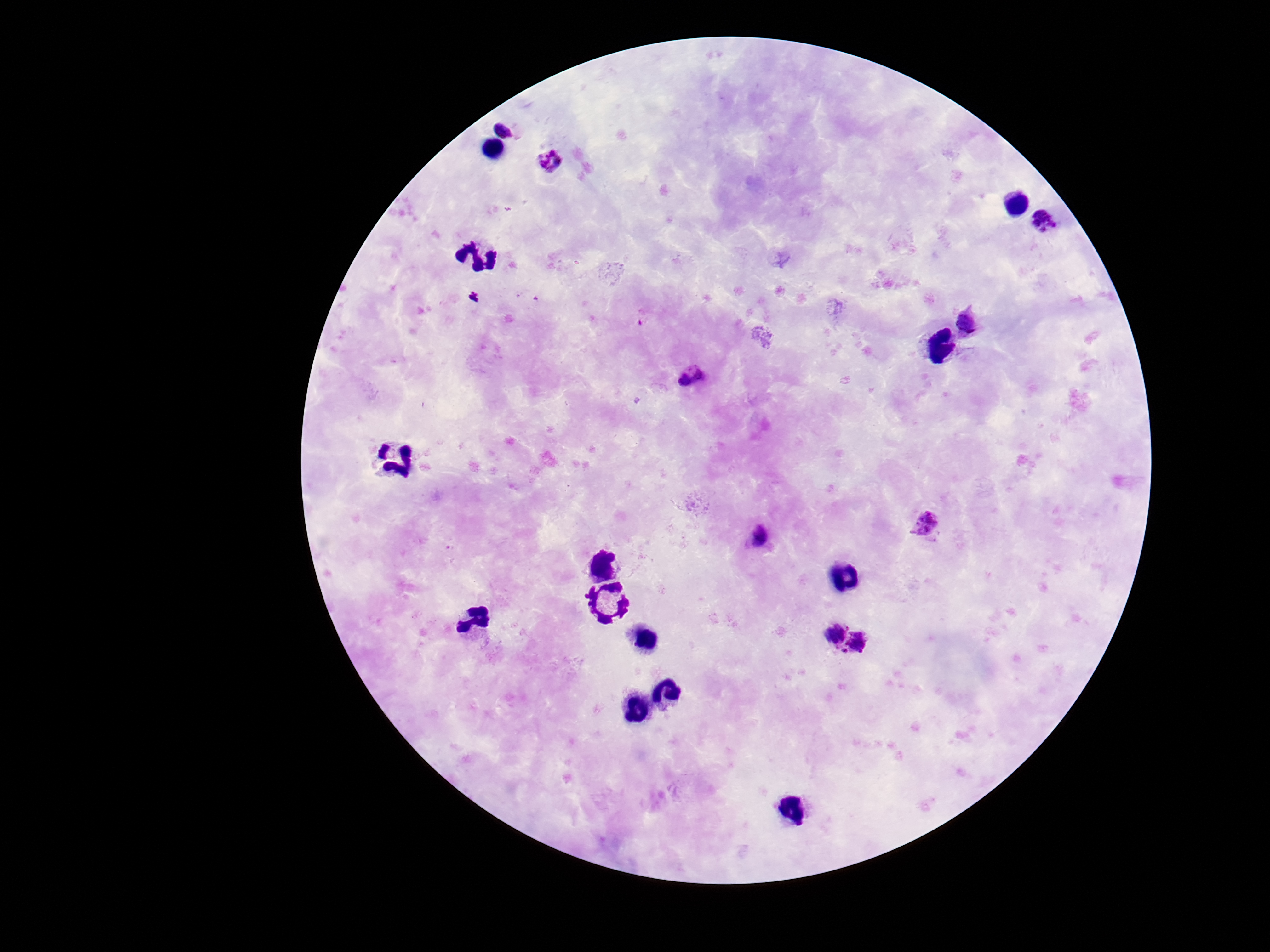
stain = Giemsa
capture = smartphone camera through the microscope eyepiece
preparation = thick peripheral-blood smear
Plasmodium parasite locations = approximate centers as [x, y] in pixels: [506, 126], [551, 163], [1048, 222], [971, 324], [692, 373], [927, 525], [762, 536], [827, 628], [864, 645]
magnification = 100x
field of view = single
image size = 1270×952 pixels
patient malaria status = positive